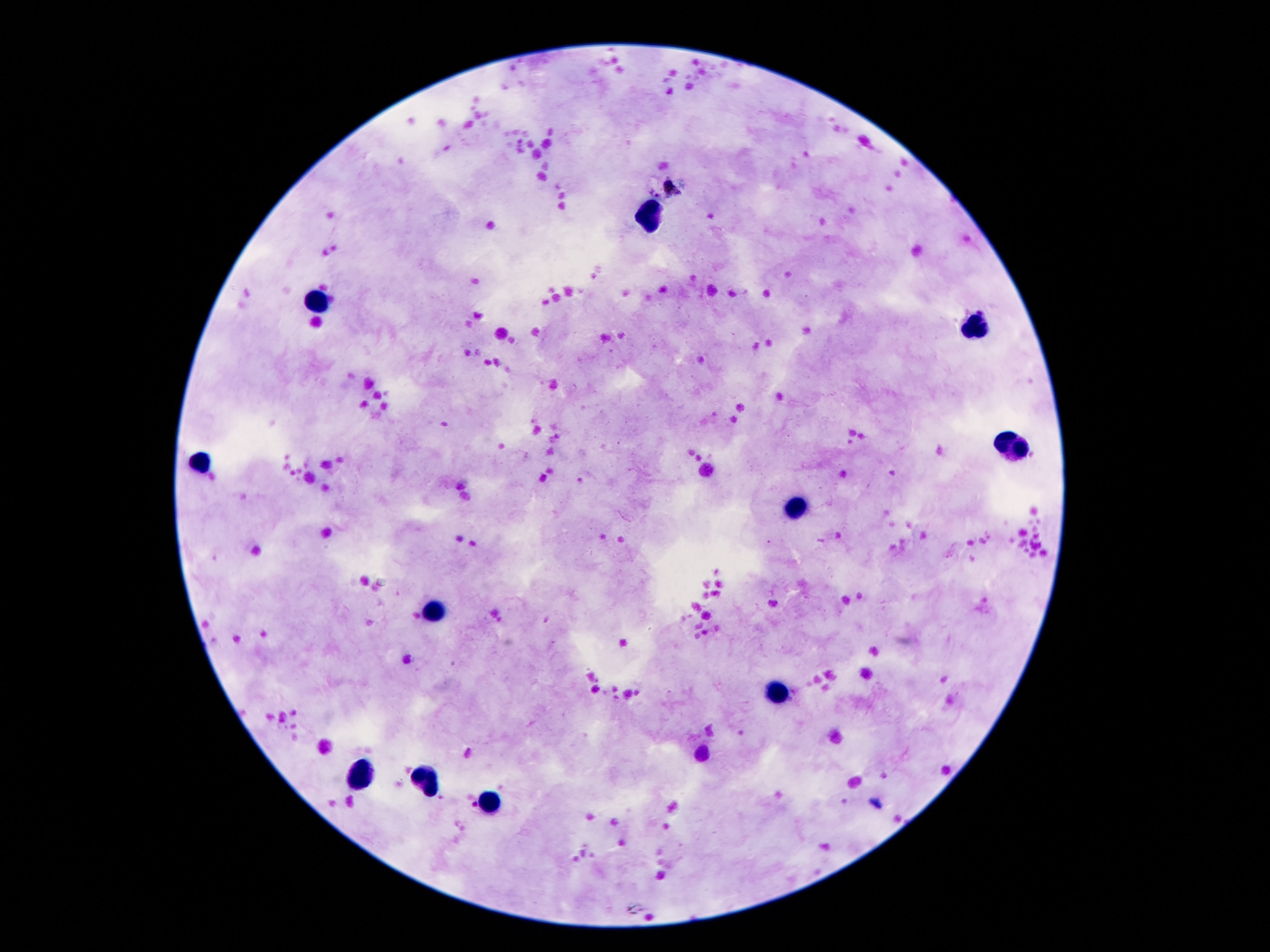

{
  "preparation": "thick peripheral-blood smear",
  "magnification": "100x",
  "patient_malaria_status": "not infected",
  "field_of_view": "single",
  "stain": "Giemsa",
  "capture": "smartphone camera through the microscope eyepiece",
  "leukocyte_locations": "approximate object centers, in pixels from the top-left corner: (x=651, y=213), (x=317, y=302), (x=977, y=326), (x=1010, y=447), (x=201, y=461), (x=799, y=509), (x=434, y=607), (x=778, y=696), (x=360, y=776), (x=428, y=778), (x=493, y=805)",
  "image_size": "1270×952 pixels"
}